Locate every Plasmodium parasite.
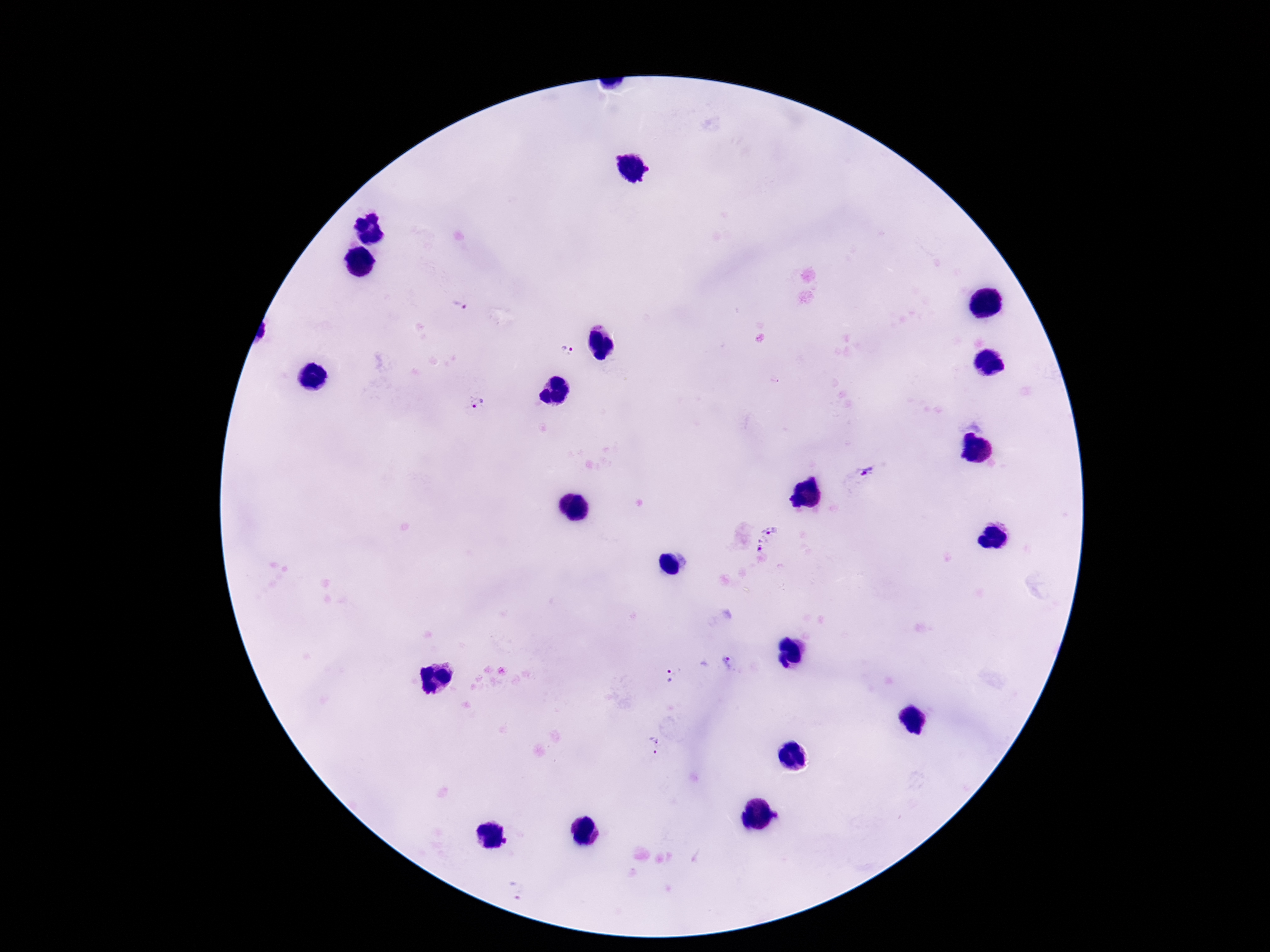

Approximate centers as [x, y] in pixels.
Plasmodium parasites: [460, 306], [568, 349], [477, 405], [868, 471], [768, 527], [764, 551], [728, 662], [674, 672], [655, 744].

Summary:
  - Capture: smartphone camera through the microscope eyepiece
  - Magnification: 100x
  - Preparation: thick blood film
  - Image size: 1270×952 pixels
  - Field of view: single
  - Stain: Giemsa
  - Patient malaria status: infected